Assess this cell for malaria.
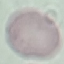
It is uninfected.

Summary:
  - Preparation: thin smear
  - Capture: smartphone camera at the microscope eyepiece
  - Stain: Giemsa
  - Image type: cell patch, automatically extracted from a larger field of view and resized to 64 × 64 pixels